Comment on the morphology of the red blood cells.
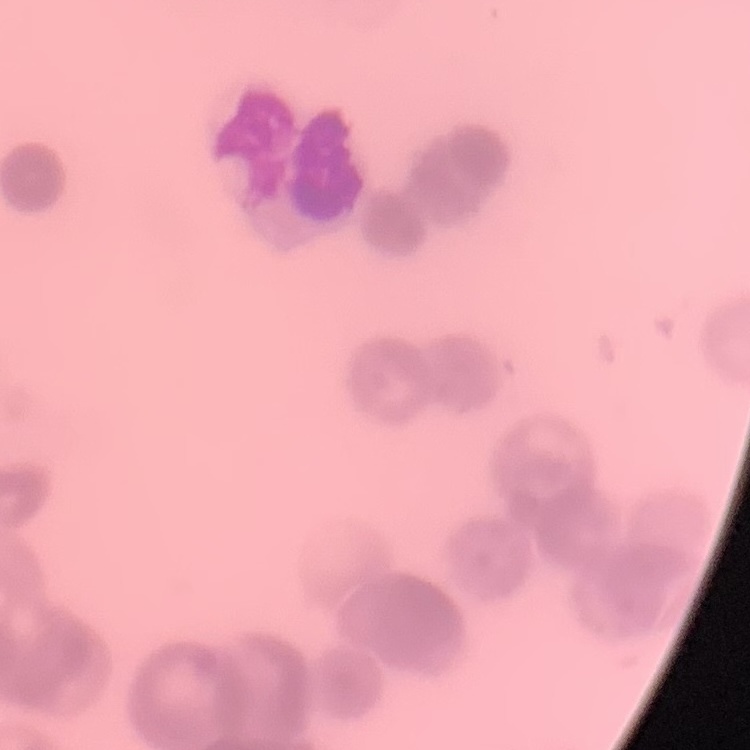

They show rouleaux formation.

Summary:
  - Preparation: thin blood film
  - Stain: Field's or Giemsa
  - Image type: square crop of a larger photomicrograph